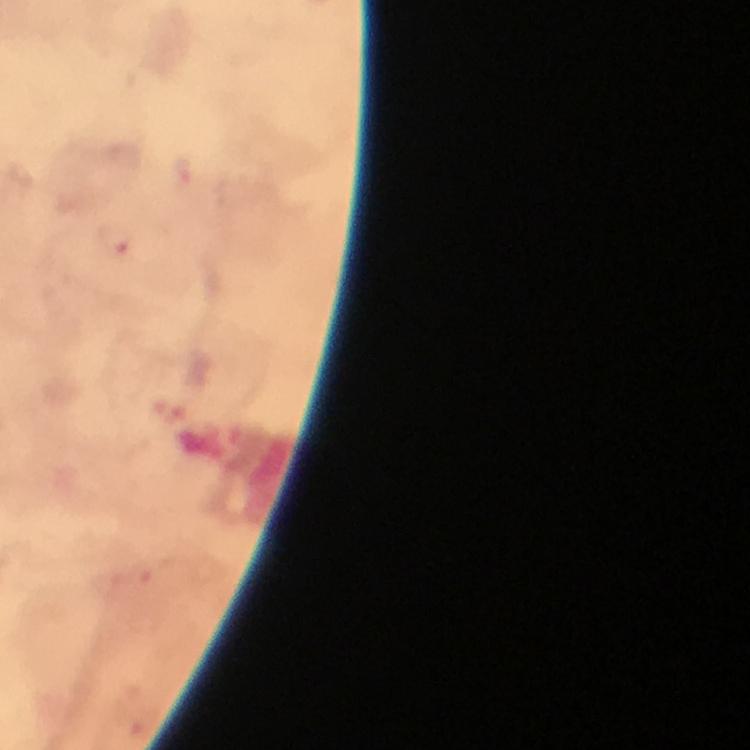

Approximate centers as [x, y] in pixels.
Summary:
  - Plasmodium parasite locations: [119, 240]
  - Magnification: 100x
  - Cropped from: one field of view
  - Stain: Giemsa
  - Image size: 750×750 pixels
  - Context: from a diagnostic examination for malaria
  - Capture: smartphone photograph through a microscope
  - Immersion oil: applied
  - Preparation: thick blood smear